Identify the cell.
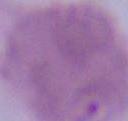

An erythrocyte.

Summary:
  - Modality: photomicrograph
  - Magnification: 1000x